Give the extent of all Plasmodium vivax-infected red blood cells.
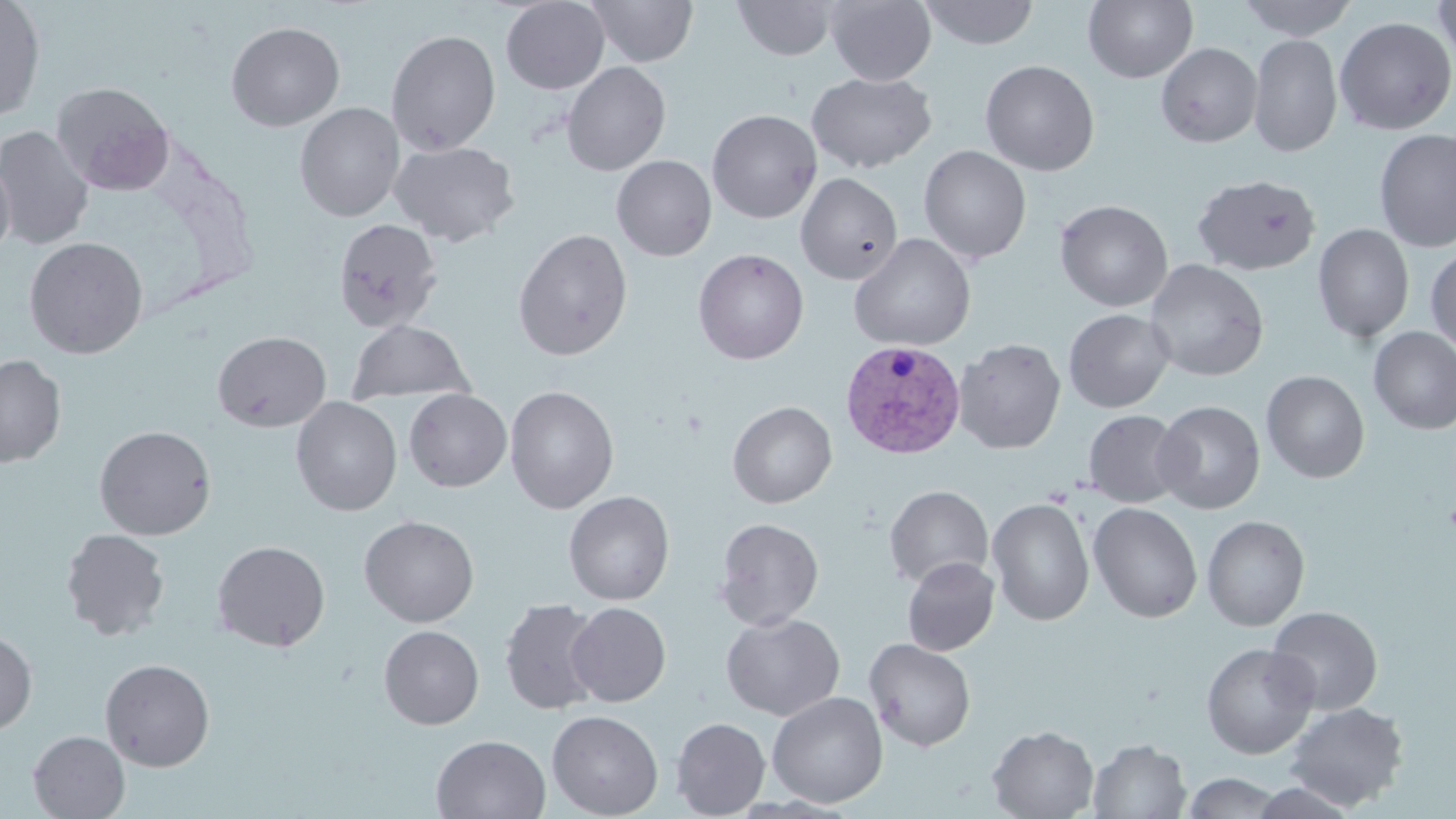

Approximate bounding boxes as (x1, y1, x2, y2) in pixels.
Plasmodium vivax-infected red blood cells: (840, 338, 967, 459).

Platelet locations: (1443, 499, 1456, 538). Uninfected red blood cell locations: (0, 0, 45, 120), (501, 0, 609, 94), (587, 0, 698, 67), (732, 0, 836, 60), (825, 0, 936, 86), (919, 0, 1039, 49), (1084, 0, 1198, 83), (1238, 0, 1357, 41), (1434, 0, 1456, 69), (1335, 17, 1455, 135), (226, 22, 345, 131), (386, 30, 501, 155), (1248, 33, 1342, 157), (1156, 42, 1262, 147), (979, 59, 1099, 176), (562, 61, 670, 176), (806, 71, 936, 173), (50, 81, 175, 195), (295, 102, 405, 221), (707, 109, 822, 224), (0, 125, 95, 249), (1374, 128, 1456, 253), (390, 140, 520, 247), (918, 145, 1032, 264), (612, 155, 716, 261), (0, 158, 16, 262), (796, 172, 903, 285), (1192, 174, 1321, 275), (1055, 199, 1173, 312), (332, 218, 442, 332), (1313, 223, 1414, 343), (512, 229, 633, 361), (848, 233, 976, 352), (24, 236, 148, 359), (1425, 246, 1456, 354), (693, 248, 809, 364), (1144, 259, 1269, 382), (1063, 309, 1174, 413), (347, 319, 475, 406), (1369, 326, 1456, 435), (212, 331, 331, 432), (953, 338, 1066, 454), (0, 354, 66, 467), (1261, 370, 1369, 483), (504, 386, 619, 513), (404, 388, 512, 492), (291, 397, 402, 516), (1153, 400, 1265, 514), (727, 401, 837, 508), (1084, 409, 1187, 507), (95, 425, 216, 540), (884, 485, 993, 589), (563, 490, 674, 605), (987, 497, 1095, 625), (1088, 502, 1202, 623), (359, 515, 480, 627), (1202, 515, 1310, 631), (714, 517, 824, 630), (60, 528, 170, 641), (211, 540, 331, 651), (902, 557, 1000, 655), (499, 598, 604, 716), (566, 602, 671, 706), (1266, 605, 1383, 715), (721, 612, 844, 721), (378, 625, 484, 729), (0, 629, 37, 735), (865, 638, 976, 751), (1201, 642, 1320, 759), (100, 658, 215, 771), (766, 691, 888, 808), (1283, 702, 1409, 811), (547, 709, 663, 818), (671, 717, 770, 818), (987, 725, 1098, 819), (28, 731, 129, 818), (431, 734, 551, 818), (1089, 738, 1190, 819), (1183, 771, 1283, 818). Slide-level diagnosis: Plasmodium vivax. Optical microscopy. Image is 1456×819 pixels. 1000x magnification. Thin blood smear. May-Grünwald-Giemsa stain. Single field of view.